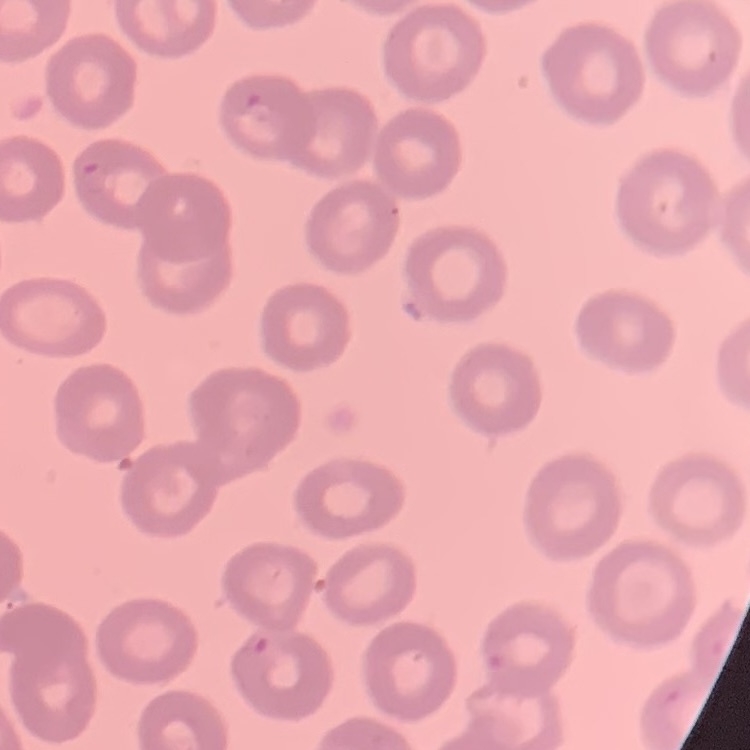

The erythrocytes exhibit no rouleaux formation. Stained with either Field's or Giemsa. One tile cut from a larger photomicrograph. Thin blood film.